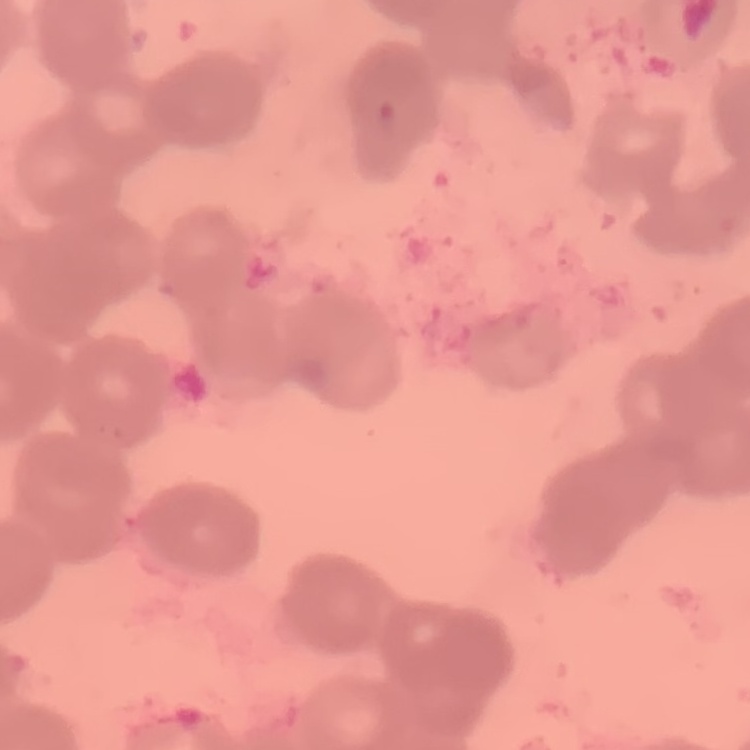 The red blood cells show rouleaux formation. Thin peripheral smear. Field's or Giemsa stain. One tile cut from a larger photomicrograph.